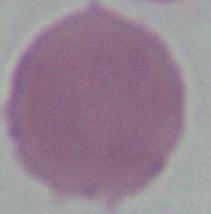

modality: micrograph
identification: erythrocyte
magnification: 1000x